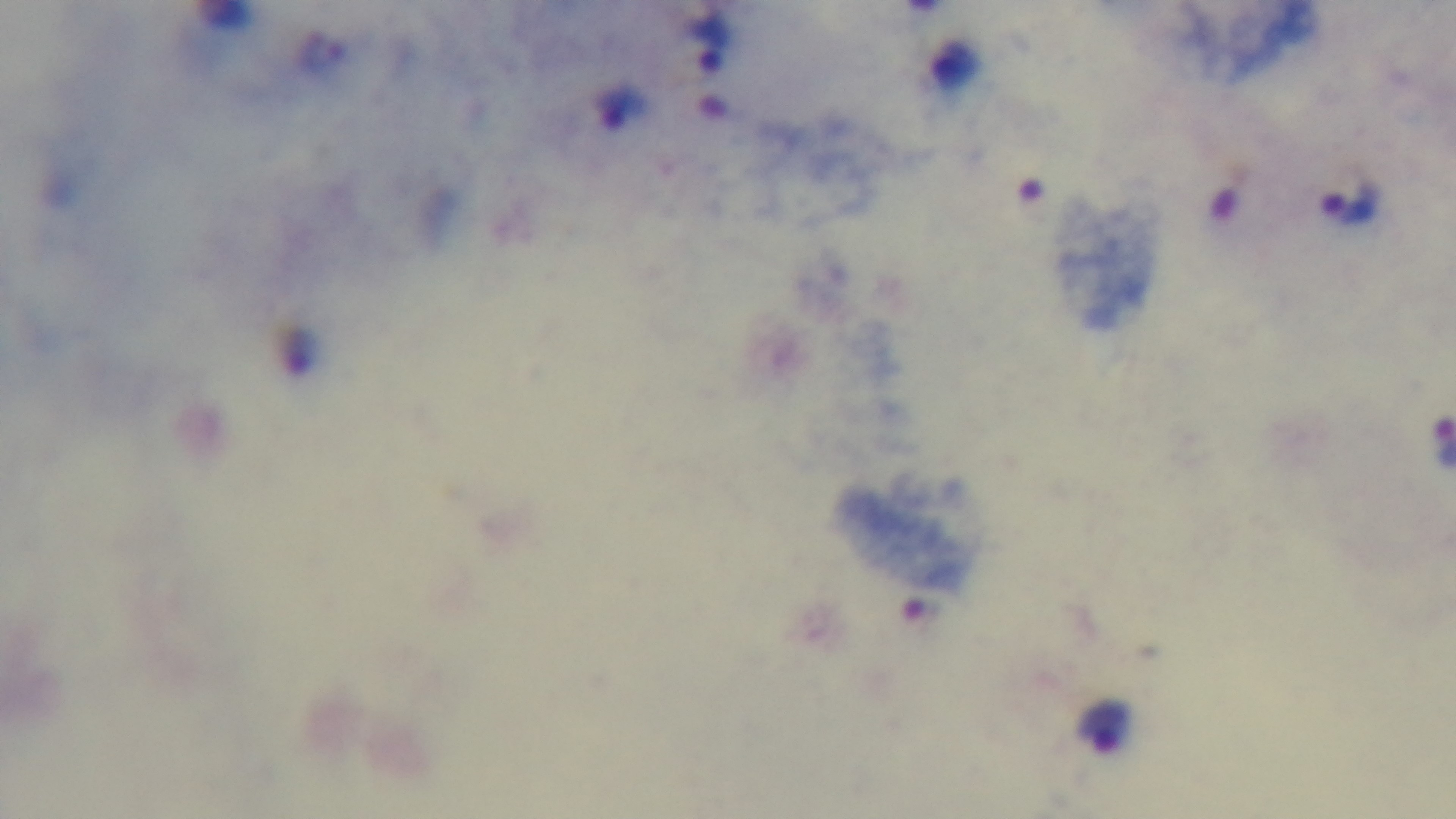
{
  "objective": "100x oil immersion",
  "field_of_view": "single",
  "modality": "light microscopy",
  "stain": "Giemsa",
  "preparation": "thick",
  "malaria_status": "infected",
  "capture": "mounted 4K digital camera"
}